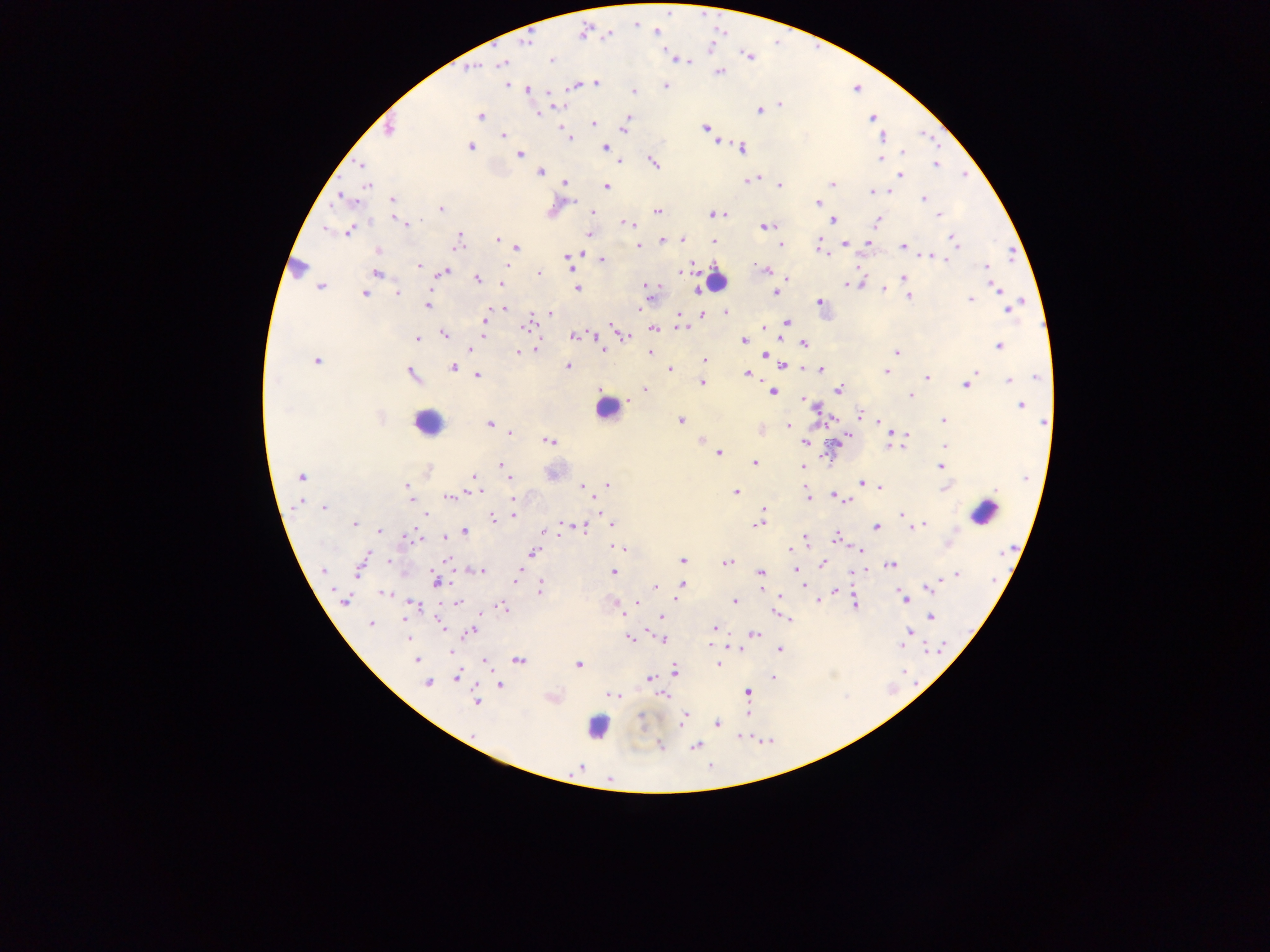 Approximate centers as [x, y] in pixels. Leukocyte locations: [717, 279], [605, 409], [427, 423], [984, 512], [598, 726]. Malaria parasite locations: [656, 32], [583, 33], [608, 35], [523, 41], [749, 57], [677, 58], [551, 59], [683, 59], [501, 63], [470, 68], [720, 72], [507, 84], [596, 84], [574, 85], [665, 85], [527, 90], [633, 91], [550, 94], [555, 105], [779, 105], [759, 109], [628, 113], [536, 114], [480, 116], [871, 118], [593, 124], [624, 128], [705, 128], [389, 129], [503, 135], [569, 137], [883, 137], [716, 141], [470, 147], [604, 147], [742, 147], [902, 153], [519, 154], [881, 158], [617, 162], [653, 162], [935, 163], [362, 165], [540, 171], [900, 176], [753, 179], [564, 183], [366, 185], [779, 185], [832, 185], [605, 186], [887, 191], [871, 192], [924, 199], [345, 200], [393, 201], [818, 203], [440, 209], [593, 211], [657, 211], [725, 214], [712, 215], [938, 215], [393, 218], [831, 220], [876, 221], [627, 223], [407, 224], [630, 226], [765, 226], [326, 227], [349, 230], [589, 234], [458, 239], [681, 239], [953, 239], [497, 240], [713, 240], [662, 241], [867, 242], [845, 243], [780, 244], [638, 245], [819, 247], [903, 247], [516, 248], [583, 250], [378, 251], [1010, 253], [931, 256], [568, 257], [602, 258], [418, 264], [859, 265], [506, 266], [986, 267], [296, 268], [767, 270], [444, 272], [377, 273], [678, 273], [538, 274], [788, 277], [903, 277], [477, 279], [861, 282], [501, 283], [845, 284], [320, 286], [648, 287], [996, 287], [576, 288], [696, 289], [884, 289], [397, 292], [650, 292], [775, 292], [364, 293], [908, 296], [970, 298], [819, 302], [427, 305], [641, 306], [504, 308], [1008, 308], [639, 311], [726, 312], [550, 313], [701, 313], [677, 316], [485, 319], [785, 321], [526, 327], [682, 327], [764, 327], [614, 328], [653, 329], [444, 333], [573, 335], [595, 335], [626, 336], [483, 337], [417, 339], [743, 340], [803, 343], [998, 345], [471, 349], [535, 349], [603, 349], [518, 352], [649, 352], [896, 352], [765, 354], [316, 360], [704, 362], [784, 366], [453, 367], [566, 367], [669, 368], [805, 368], [820, 369], [976, 370], [886, 371], [410, 374], [746, 374], [477, 375], [1036, 376], [926, 377], [1009, 379], [701, 382], [965, 384], [839, 389], [646, 390], [772, 391], [909, 394], [803, 399], [629, 400], [807, 402], [1020, 405], [861, 414], [832, 419], [680, 420], [943, 421], [878, 422], [1044, 422], [488, 423], [787, 426], [760, 430], [895, 432], [510, 433], [908, 434], [843, 437], [701, 439], [550, 441], [805, 441], [901, 445], [889, 446], [945, 446], [718, 453], [754, 462], [502, 464], [803, 466], [941, 466], [301, 477], [473, 477], [509, 478], [860, 482], [606, 485], [583, 487], [944, 487], [879, 488], [407, 489], [735, 491], [470, 492], [805, 492], [832, 495], [513, 496], [450, 497], [807, 497], [843, 498], [411, 500], [848, 501], [323, 507], [596, 508], [764, 510], [599, 512], [426, 514], [900, 514], [513, 515], [762, 515], [492, 518], [562, 523], [354, 524], [758, 524], [613, 525], [922, 525], [915, 526], [578, 527], [876, 527], [910, 527], [465, 530], [380, 531], [543, 532], [410, 537], [444, 537], [416, 538], [806, 538], [835, 538], [948, 543], [619, 547], [788, 550], [859, 550], [533, 553], [447, 559], [682, 560], [389, 561], [361, 563], [727, 563], [890, 564], [823, 565], [796, 568], [481, 570], [322, 571], [519, 572], [613, 572], [760, 572], [956, 575], [516, 577], [436, 580], [515, 582], [681, 584], [804, 584], [655, 586], [539, 587], [927, 587], [680, 590], [761, 590], [836, 590], [384, 593], [780, 597], [904, 597], [344, 599], [818, 600], [734, 601], [458, 602], [614, 602], [637, 602], [854, 603], [413, 605], [502, 608], [620, 611], [774, 613], [662, 616], [930, 617], [789, 620], [439, 622], [370, 624], [442, 627], [714, 628], [647, 629], [909, 630], [470, 632], [754, 633], [409, 638], [629, 639], [662, 639], [730, 646], [901, 646], [738, 648], [780, 649], [449, 652], [417, 660], [518, 660], [484, 662], [717, 664], [578, 665], [673, 670], [457, 676], [772, 677], [649, 679], [427, 683], [499, 685], [747, 692], [612, 693], [662, 695], [476, 701], [747, 713], [683, 716], [716, 723], [474, 734], [660, 746], [695, 746], [580, 767]. Single field of view. Image is 1270×952 pixels. Mobile-phone photograph taken through the microscope. Thick blood smear. Sample from Ghana.